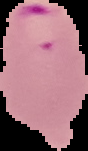
Cell region segmented out of the field of view; the surrounding area is masked to black. From a thin blood film. Malaria status: parasitized. Image is 88×151 pixels.